Locate every malaria parasite.
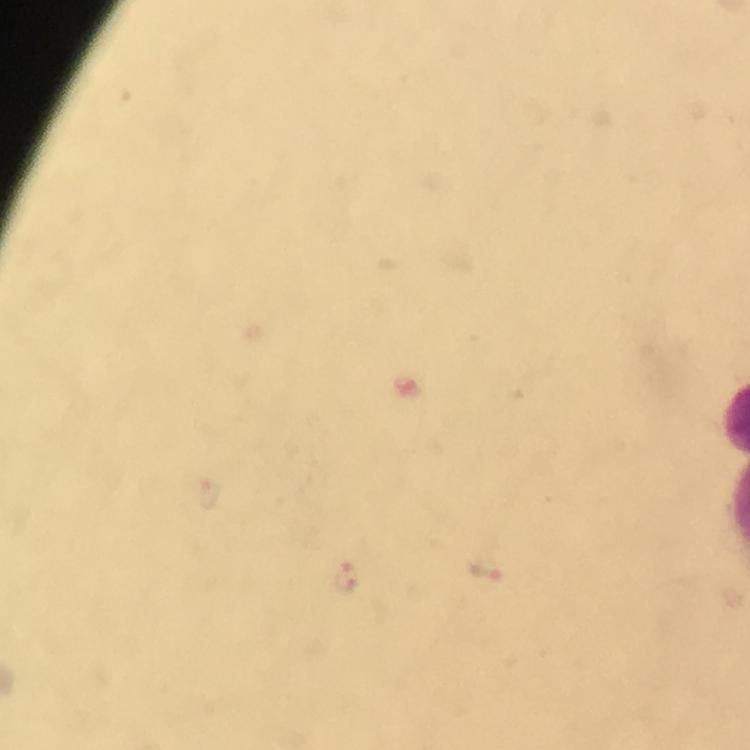

Approximate centers as (x, y) in pixels.
Malaria parasites: (211, 495), (483, 569), (345, 580).

At 100x magnification. Immersion oil applied. From a diagnostic examination for malaria. Photographed through the microscope with a smartphone camera. Giemsa stain. Image is 750×750 pixels. Thick smear. Cropped region of a single field of view.